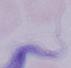
A trypanosome is seen. 1000x magnification. Micrograph.